State which cell type is depicted.
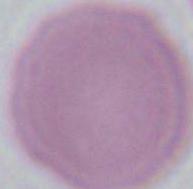

This is an erythrocyte.

{
  "modality": "micrograph",
  "magnification": "1000x"
}